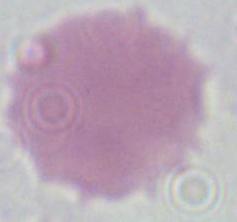
A red blood cell is seen. Micrograph. 1000x magnification.